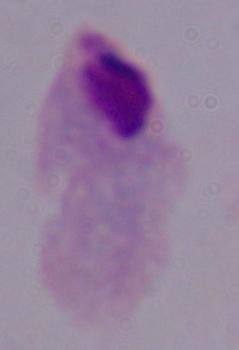

magnification = 1000x
identification = trichomonad
modality = photomicrograph